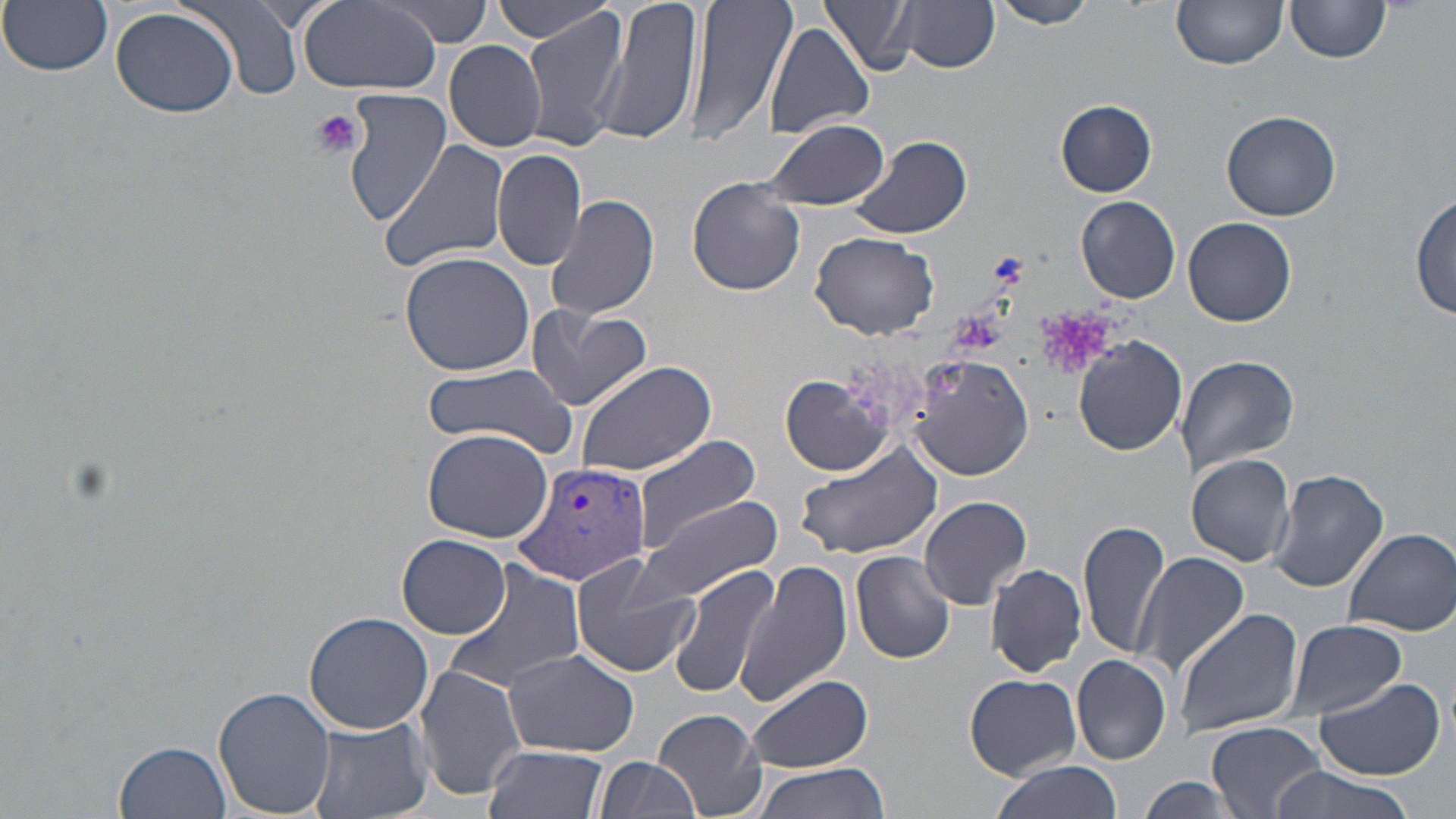
Summary:
  - Coordinate format: approximate bounding boxes as [x1, y1, x2, y2] in pixels
  - Platelet locations: [310, 107, 365, 159]
  - Uninfected red blood cell locations: [4, 0, 114, 76], [186, 0, 306, 102], [487, 0, 623, 44], [595, 0, 700, 149], [687, 0, 797, 147], [822, 0, 920, 77], [989, 0, 1097, 29], [1173, 0, 1288, 71], [299, 2, 442, 94], [378, 2, 498, 44], [899, 2, 999, 74], [1285, 2, 1391, 66], [786, 5, 901, 109], [111, 6, 240, 119], [522, 9, 628, 152], [765, 24, 875, 136], [428, 33, 539, 243], [445, 39, 547, 151], [342, 89, 451, 224], [1055, 100, 1159, 197], [1221, 109, 1341, 221], [761, 119, 890, 211], [845, 135, 973, 241], [379, 136, 514, 274], [493, 145, 586, 272], [687, 179, 806, 296], [1412, 191, 1456, 324], [547, 194, 660, 321], [1075, 196, 1182, 304], [1182, 216, 1297, 326], [810, 233, 940, 341], [398, 249, 536, 376], [526, 305, 651, 412], [1074, 336, 1188, 456], [1174, 353, 1300, 479], [908, 354, 1034, 481], [574, 359, 717, 477], [423, 366, 577, 455], [781, 375, 893, 476], [422, 427, 554, 543], [625, 432, 763, 549], [791, 441, 945, 558], [1185, 454, 1296, 567], [1269, 469, 1388, 592], [918, 495, 1033, 610], [632, 498, 783, 606], [1078, 519, 1170, 661], [1340, 526, 1456, 636], [398, 534, 512, 638], [851, 549, 955, 664], [1132, 552, 1249, 679], [570, 557, 699, 677], [442, 560, 587, 692], [985, 562, 1087, 677], [737, 563, 852, 709], [667, 564, 782, 699], [1173, 608, 1303, 738], [303, 612, 435, 734], [1282, 620, 1406, 723], [501, 649, 642, 758], [1072, 655, 1173, 764], [413, 665, 525, 802], [744, 673, 875, 776], [965, 673, 1080, 779], [1308, 675, 1447, 780], [213, 686, 336, 817], [652, 708, 767, 817], [305, 717, 434, 819], [1206, 721, 1326, 817], [115, 740, 234, 819], [483, 745, 608, 819], [593, 757, 699, 819], [748, 761, 889, 819], [990, 763, 1122, 819], [1264, 763, 1417, 819], [1134, 777, 1239, 815]
  - Plasmodium vivax-infected red blood cell locations: [512, 461, 651, 587]
  - Slide-level diagnosis: Plasmodium vivax
  - Stain: May-Grünwald-Giemsa
  - Modality: light microscopy
  - Preparation: thin blood smear
  - Field of view: one of a larger specimen
  - Magnification: 1000x
  - Image size: 1456×819 pixels